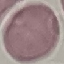

result: no malaria parasites seen
capture: smartphone camera at the microscope eyepiece
image_type: cell patch, automatically extracted from a larger field of view and resized to 64 × 64 pixels
preparation: thin smear
stain: Giemsa